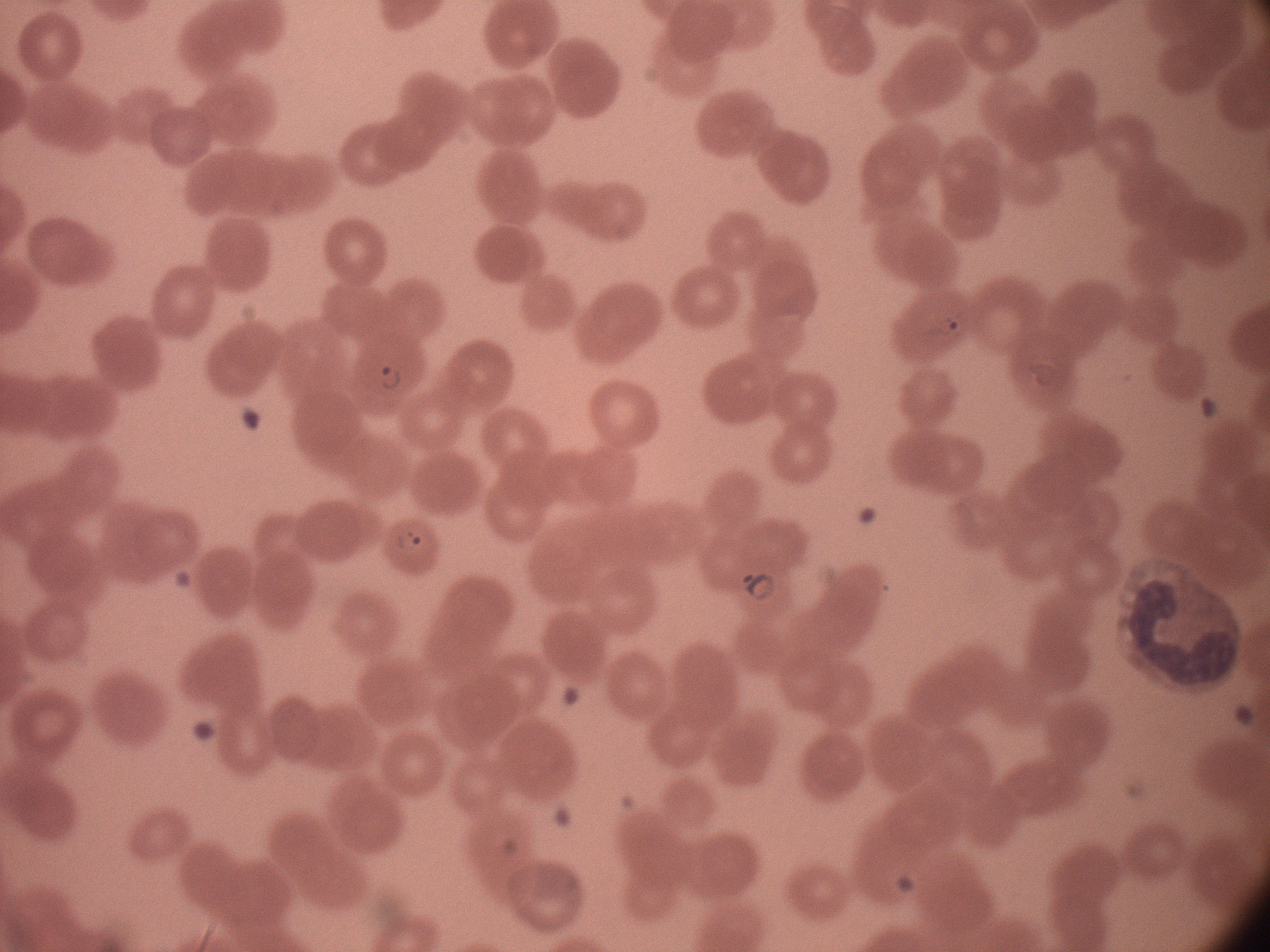 Approximate bounding boxes as (x1,y1)-(x2,y2) corner pairs in pixels, from the source annotation, which is not necessarily exhaustive. Ring form locations: (920,300)-(980,353), (369,357)-(417,403), (387,518)-(438,561), (736,563)-(783,608). Acquired with a Leica DM2000 optical microscope and its built-in camera. Captured at 100x magnification. Species: Plasmodium falciparum. One field from this slide. Giemsa-stained preparation. Thin blood smear. Image is 1270×952 pixels.